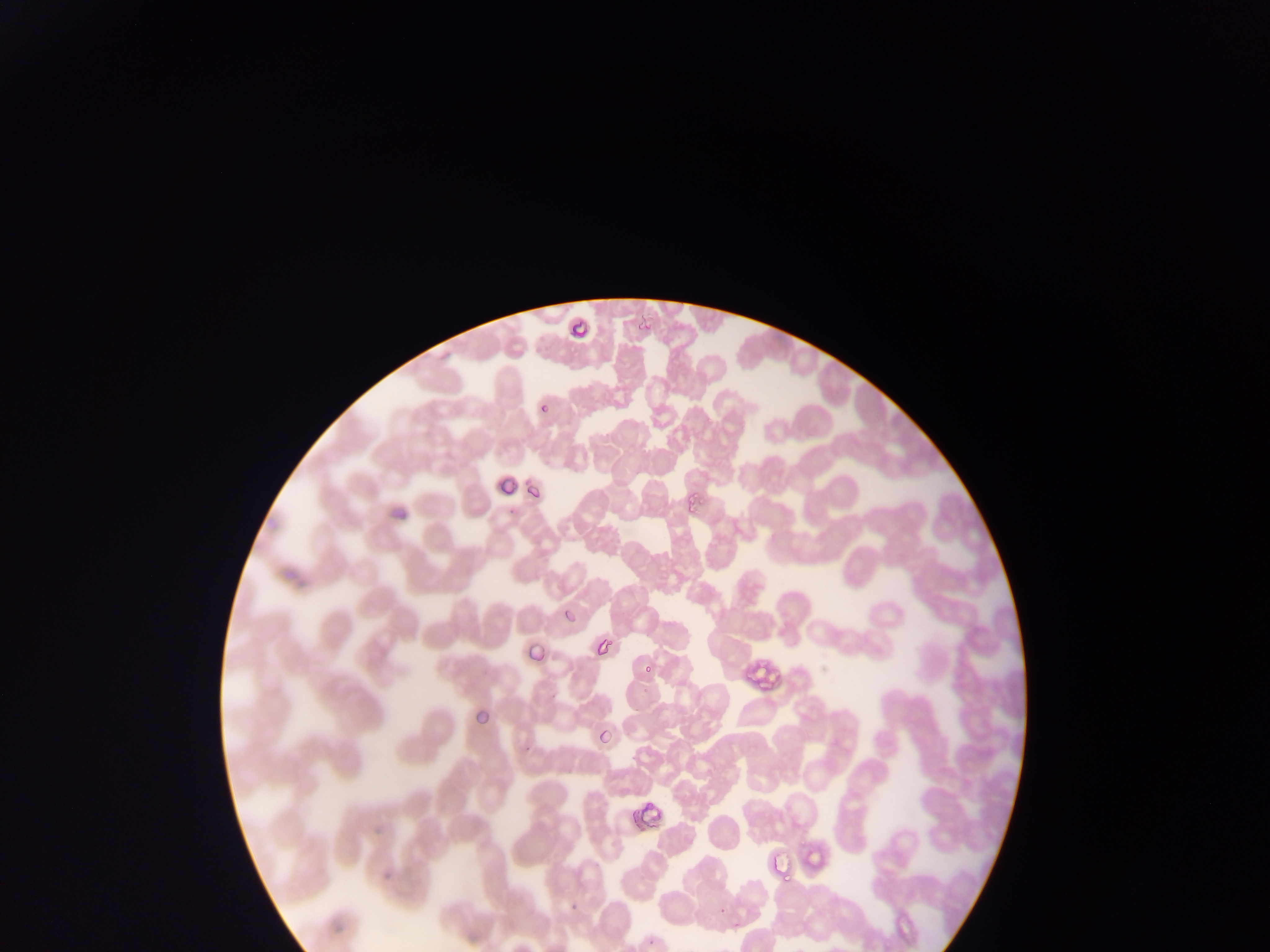 Approximate bounding boxes as [left, top, right, bottom] in pixels. Plasmodium parasite locations: [568, 314, 591, 336], [636, 315, 659, 333], [530, 393, 558, 425], [497, 467, 511, 504], [521, 474, 541, 502], [675, 481, 719, 517], [381, 496, 412, 533], [559, 605, 592, 625], [590, 637, 617, 659], [521, 645, 551, 667], [741, 654, 778, 689], [639, 663, 661, 673], [465, 697, 498, 736], [590, 722, 620, 753], [629, 790, 680, 839], [763, 845, 796, 888], [806, 845, 834, 869], [378, 863, 399, 890], [567, 901, 582, 912], [714, 902, 733, 919], [327, 912, 350, 952], [644, 933, 663, 949]. Mobile-phone photograph taken through the microscope. Image is 1270×952 pixels. Single field of view. Thin blood smear. Collected in Ghana.